Assess this cell for malaria.
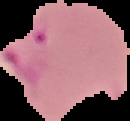

Parasitized.

Summary:
  - Preparation: thin blood smear
  - Image type: cell region segmented out of the field of view; surrounding area masked to black
  - Image size: 130×121 pixels